Assess the morphology of the red blood cells.
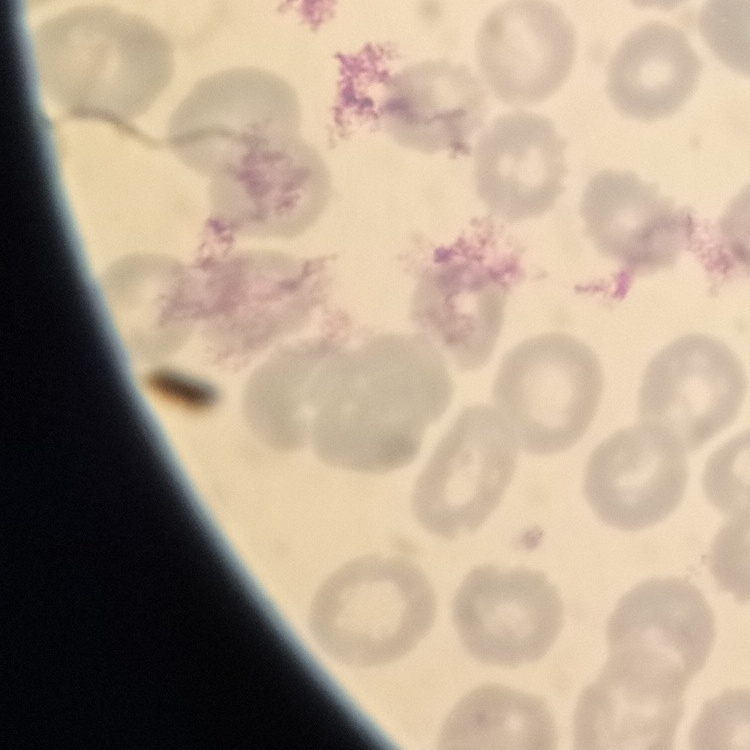
No rouleaux formation.

Summary:
  - Preparation: thin peripheral smear
  - Image type: one tile cut from a larger photomicrograph
  - Stain: Field's or Giemsa